Assess this cell for malaria.
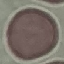

It is uninfected.

capture = smartphone camera at the microscope eyepiece
stain = Giemsa
image type = automatically extracted cell patch, resized to 64 × 64 pixels
preparation = thin blood film